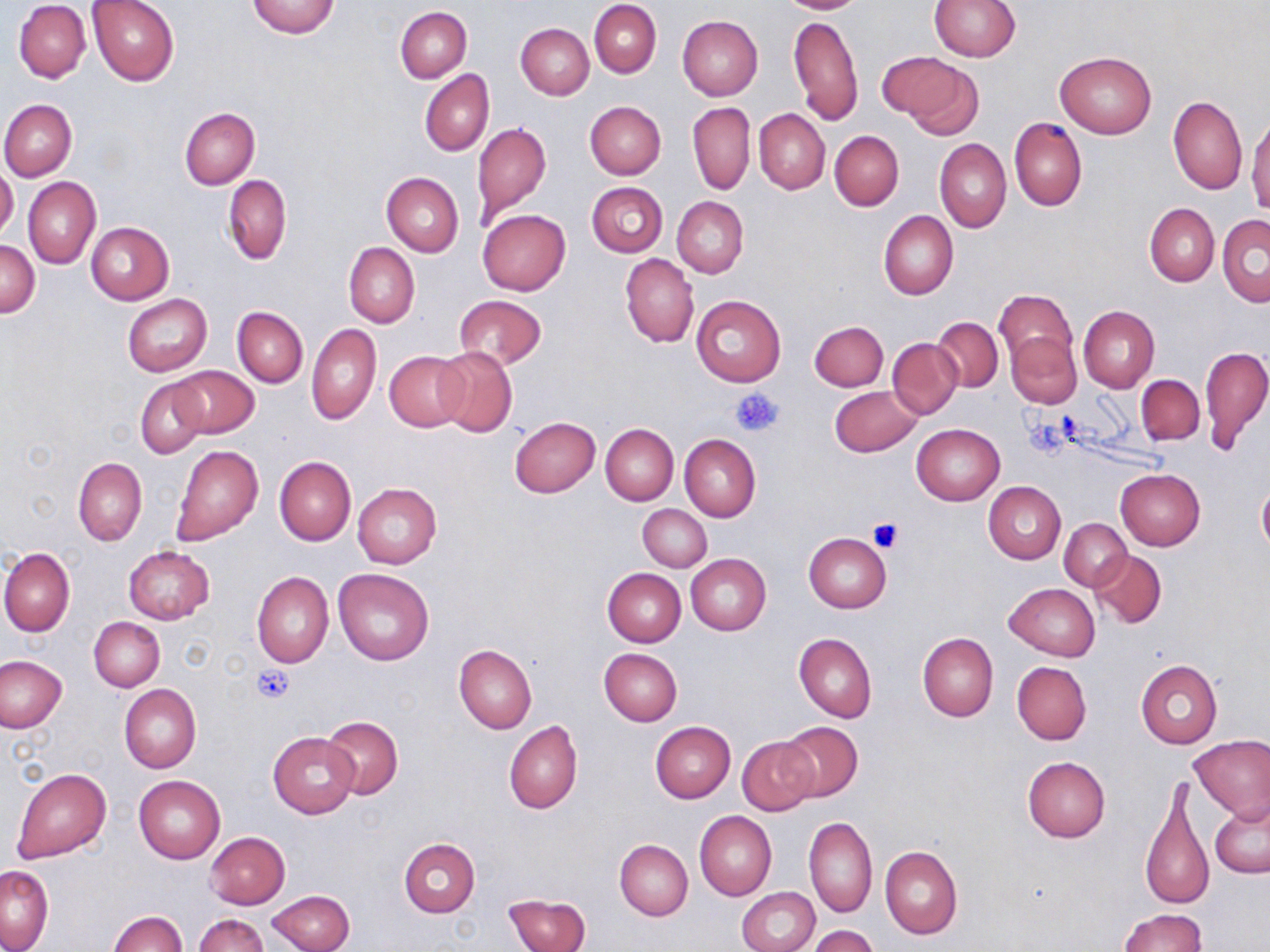
slide-level diagnosis = negative for blood parasites
magnification = 1000x
uninfected red blood cell locations = approximate bounding boxes as (x1,y1)-(x2,y2) corner pairs in pixels: (87,0)-(179,85), (779,0)-(864,14), (929,0)-(1019,61), (247,1)-(340,38), (590,1)-(661,77), (14,2)-(91,82), (396,7)-(472,82), (789,13)-(862,126), (519,14)-(661,88), (677,15)-(763,100), (516,22)-(593,99), (1055,51)-(1156,138), (876,53)-(971,130), (419,70)-(494,157), (1168,96)-(1247,194), (1,99)-(76,180), (585,101)-(666,179), (687,102)-(755,195), (180,108)-(259,189), (754,109)-(829,194), (1247,113)-(1269,214), (1010,117)-(1086,211), (472,122)-(551,222), (829,130)-(904,211), (935,139)-(1012,232), (0,165)-(18,240), (382,171)-(463,256), (223,175)-(292,264), (22,177)-(100,270), (586,182)-(668,256), (672,196)-(748,278), (1145,203)-(1219,286), (477,209)-(571,295), (878,210)-(958,301), (1217,215)-(1270,306), (86,222)-(174,305), (1,242)-(39,317), (343,244)-(419,327), (620,253)-(699,349), (994,290)-(1078,367), (122,294)-(212,376), (690,294)-(786,386), (455,296)-(547,368), (1078,305)-(1159,393), (232,307)-(308,387), (932,317)-(1003,392), (810,320)-(888,391), (307,322)-(381,426), (1006,332)-(1082,409), (887,338)-(962,418), (1200,344)-(1270,455), (435,346)-(518,437), (385,352)-(470,431), (168,365)-(258,438), (1137,374)-(1204,444), (135,378)-(208,459), (829,385)-(923,458), (510,416)-(601,498), (601,423)-(678,505), (912,423)-(1004,504), (679,434)-(760,522), (173,446)-(264,546), (273,457)-(355,546), (73,458)-(147,546), (1115,468)-(1205,549), (983,481)-(1066,564), (352,483)-(441,568), (1257,484)-(1270,556), (638,504)-(711,571), (1059,517)-(1131,590), (804,532)-(892,612), (123,547)-(215,624), (0,548)-(74,636), (1090,549)-(1166,628), (686,554)-(770,635), (334,567)-(434,665), (602,567)-(686,646), (252,572)-(333,668), (1004,583)-(1098,662), (89,618)-(164,691), (794,632)-(877,722), (917,632)-(998,721), (454,645)-(536,734), (599,648)-(682,726), (1,655)-(67,732), (1135,659)-(1221,749), (1012,661)-(1091,745), (119,684)-(201,772), (320,715)-(402,800), (504,720)-(582,814), (651,721)-(735,804), (777,721)-(863,802), (268,732)-(359,817), (1189,734)-(1270,823), (737,735)-(819,816), (1022,755)-(1110,843), (12,767)-(110,863), (134,776)-(224,863), (1141,780)-(1213,913), (1210,801)-(1270,879), (695,811)-(776,901), (804,816)-(877,918), (205,832)-(290,909), (399,839)-(480,917), (615,839)-(693,920), (881,844)-(962,940), (1,866)-(54,951), (739,887)-(820,952), (268,890)-(356,952), (504,894)-(590,952), (1118,908)-(1207,952), (110,910)-(187,951), (193,914)-(268,952), (809,926)-(879,952)
image size = 1270×952 pixels
preparation = thin blood smear
field of view = one of a larger specimen
platelet locations = approximate bounding boxes as (x1,y1)-(x2,y2) corner pairs in pixels: (731,387)-(783,437), (1022,411)-(1078,458), (869,519)-(903,553), (251,665)-(295,704)
modality = optical microscopy
stain = May-Grünwald-Giemsa